Outline each blood parasite and name the species.
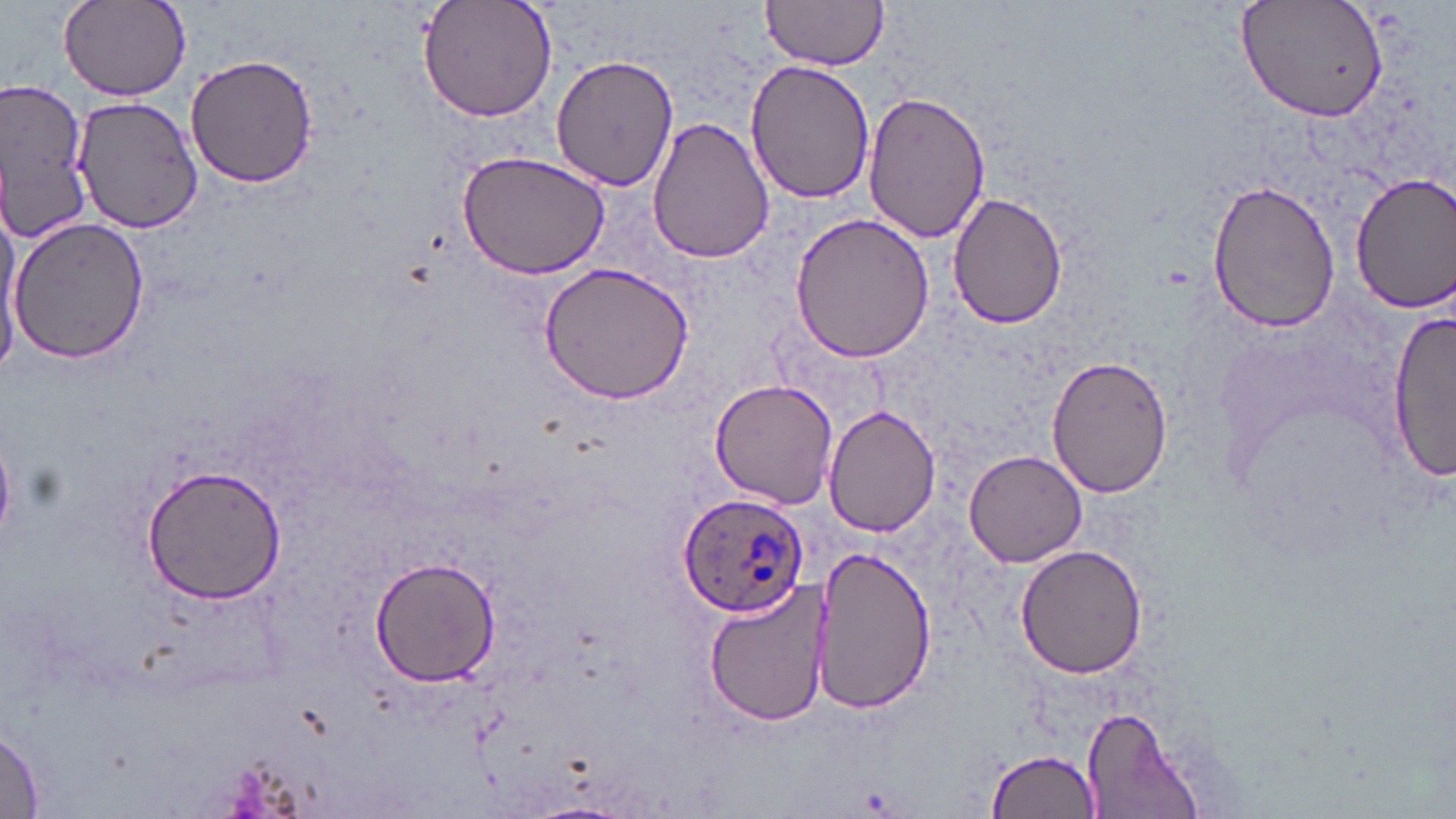
Approximate bounding boxes as (x1,y1)-(x2,y2) corner pairs in pixels.
Plasmodium ovale-infected red blood cells: (677,491)-(808,616).
No Plasmodium falciparum, Plasmodium malariae, Plasmodium vivax, Babesia divergens, or Trypanosoma brucei observed.

Summary:
  - Uninfected red blood cell locations: (59,0)-(192,100), (416,0)-(558,123), (760,0)-(890,71), (1238,0)-(1390,123), (185,54)-(317,189), (549,54)-(680,193), (745,59)-(877,202), (2,79)-(91,247), (863,90)-(990,244), (76,96)-(203,232), (647,116)-(774,264), (458,151)-(610,280), (1349,172)-(1456,312), (1209,179)-(1343,331), (946,191)-(1070,328), (1,205)-(25,372), (789,213)-(938,364), (8,215)-(150,364), (536,261)-(697,405), (1388,311)-(1454,483), (1047,354)-(1172,499), (709,376)-(840,507), (823,405)-(941,537), (964,449)-(1087,568), (139,463)-(287,605), (1015,545)-(1147,679), (813,548)-(935,712), (371,556)-(499,685), (705,580)-(831,731), (1082,707)-(1199,819), (0,721)-(45,818), (985,748)-(1100,818), (520,803)-(635,819)
  - Slide-level diagnosis: Plasmodium ovale
  - Image size: 1456×819 pixels
  - Field of view: one of a larger specimen
  - Magnification: 1000x
  - Modality: light microscopy
  - Preparation: thin blood smear
  - Stain: May-Grünwald-Giemsa